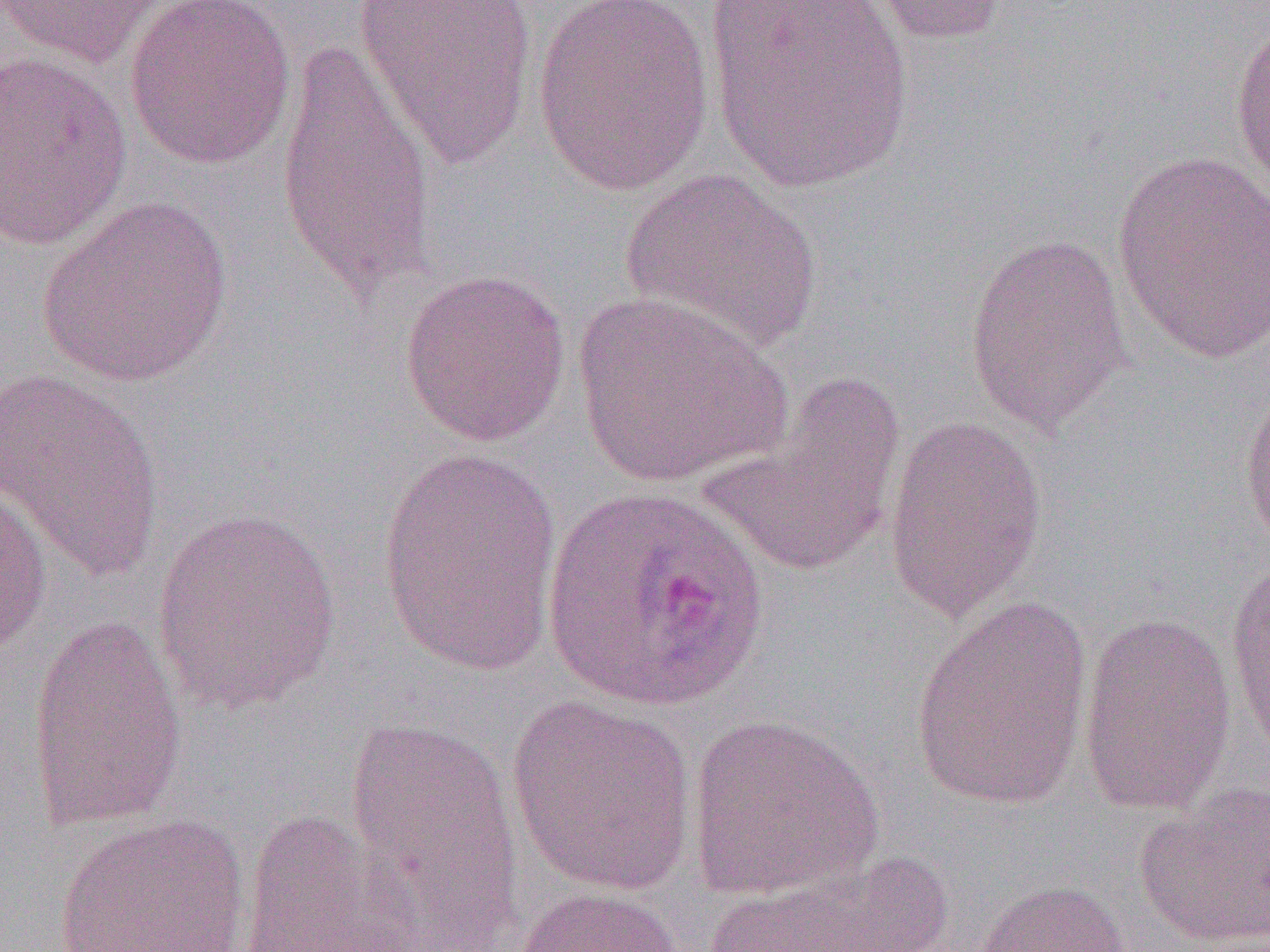
Summary:
  - Coordinate format: approximate bounding boxes as (x1, y1, x2, y2) in pixels
  - Uninfected red blood cell locations: (0, 0, 173, 69), (123, 0, 298, 170), (353, 0, 538, 170), (531, 0, 715, 197), (704, 0, 912, 192), (857, 0, 1014, 46), (1230, 17, 1270, 199), (276, 32, 437, 311), (1, 50, 134, 250), (1110, 150, 1270, 366), (619, 169, 824, 358), (37, 196, 234, 387), (963, 231, 1133, 438), (399, 268, 571, 447), (571, 291, 791, 488), (0, 369, 166, 585), (699, 372, 907, 576), (1238, 378, 1270, 552), (884, 414, 1049, 627), (375, 446, 563, 674), (0, 476, 53, 657), (150, 507, 344, 717), (1224, 551, 1270, 763), (909, 594, 1094, 814), (1078, 611, 1237, 816), (25, 613, 188, 830), (505, 694, 699, 898), (685, 712, 885, 902), (342, 715, 521, 936), (1133, 785, 1270, 949), (238, 809, 426, 951), (52, 812, 251, 952), (690, 855, 958, 952), (969, 878, 1133, 952), (512, 886, 684, 952)
  - Slide-level diagnosis: Plasmodium ovale
  - Modality: light microscopy
  - Preparation: thin blood film
  - Field of view: single
  - Image size: 1270×952 pixels
  - Magnification: 1000x